State the blood parasite species.
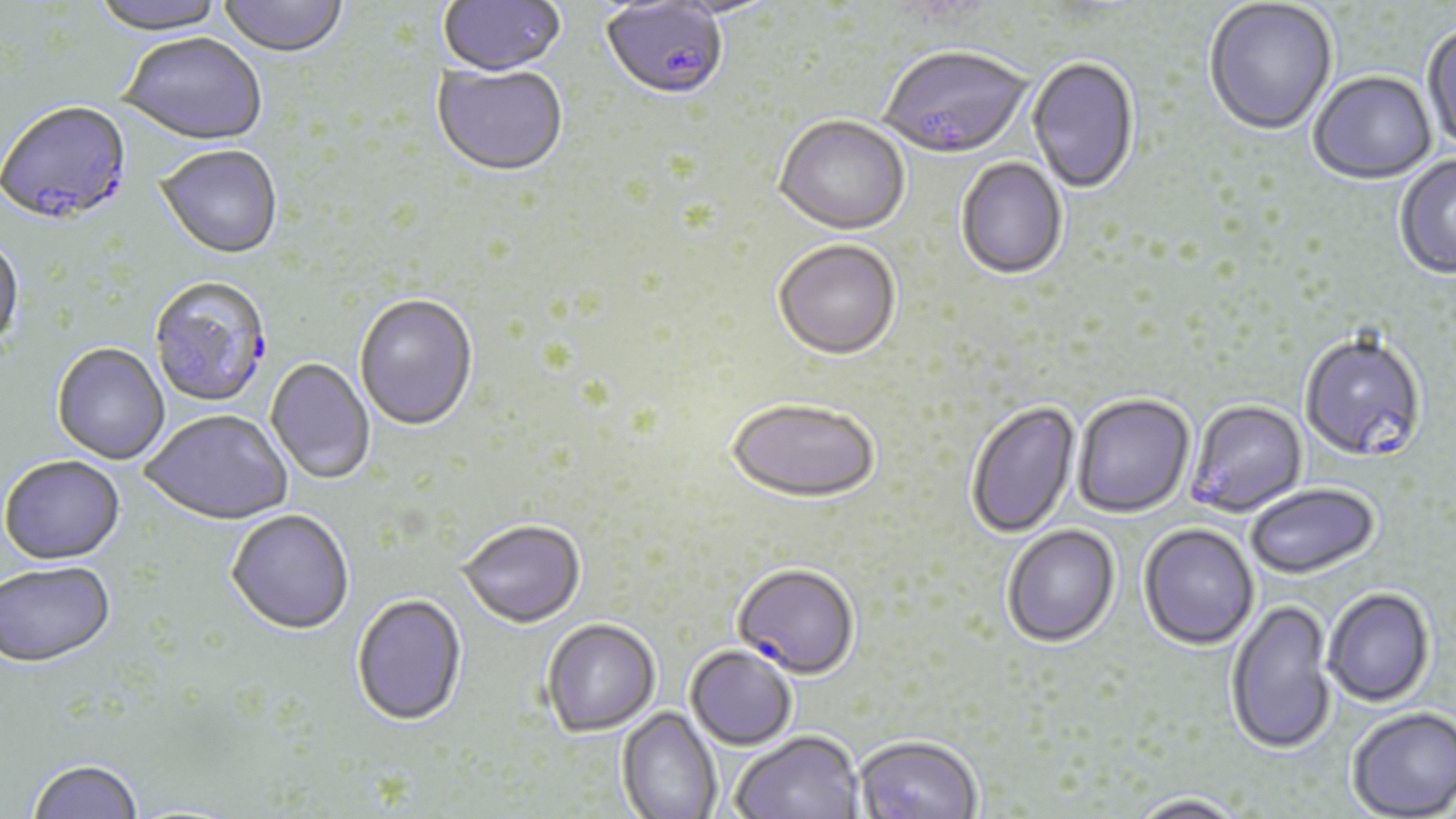
Plasmodium falciparum.

{
  "field_of_view": "single",
  "uninfected_red_blood_cell_locations": "approximate bounding boxes as [x1, y1, x2, y2] in pixels: [89, 0, 230, 37], [438, 0, 567, 79], [650, 0, 783, 22], [1204, 0, 1338, 138], [218, 1, 349, 59], [1421, 24, 1456, 157], [119, 35, 268, 148], [1026, 58, 1139, 196], [432, 65, 569, 179], [1309, 73, 1436, 186], [774, 118, 910, 238], [156, 146, 283, 262], [1395, 156, 1456, 280], [955, 159, 1067, 281], [0, 238, 25, 355], [773, 242, 901, 363], [354, 295, 478, 433], [51, 344, 170, 465], [265, 359, 375, 485], [1072, 394, 1195, 518], [726, 399, 880, 504], [966, 400, 1081, 540], [140, 413, 293, 527], [1, 457, 125, 567], [1245, 484, 1380, 578], [225, 511, 355, 637], [458, 521, 586, 630], [1138, 523, 1260, 650], [1002, 525, 1120, 647], [0, 564, 116, 670], [1322, 587, 1435, 707], [351, 596, 468, 729], [1225, 599, 1336, 755], [541, 618, 661, 737], [686, 645, 797, 750], [1346, 705, 1456, 818], [616, 707, 723, 819], [730, 730, 863, 819], [853, 734, 982, 819], [26, 760, 144, 819], [1127, 793, 1250, 819]",
  "stain": "May-Grünwald-Giemsa",
  "plasmodium_falciparum_infected_red_blood_cell_locations": "approximate bounding boxes as [x1, y1, x2, y2] in pixels: [600, 2, 728, 104], [879, 49, 1032, 162], [0, 104, 133, 229], [149, 277, 273, 410], [1299, 334, 1427, 464], [1186, 400, 1308, 517], [733, 563, 860, 679]",
  "image_size": "1456×819 pixels",
  "magnification": "1000x",
  "modality": "optical microscopy",
  "preparation": "thin blood smear"
}